Assess this cell for malaria.
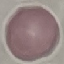
Uninfected.

Acquired by smartphone through the microscope eyepiece. Giemsa-stained preparation. Thin blood film. Cell patch, automatically extracted from a larger field of view and resized to 64 × 64 pixels.